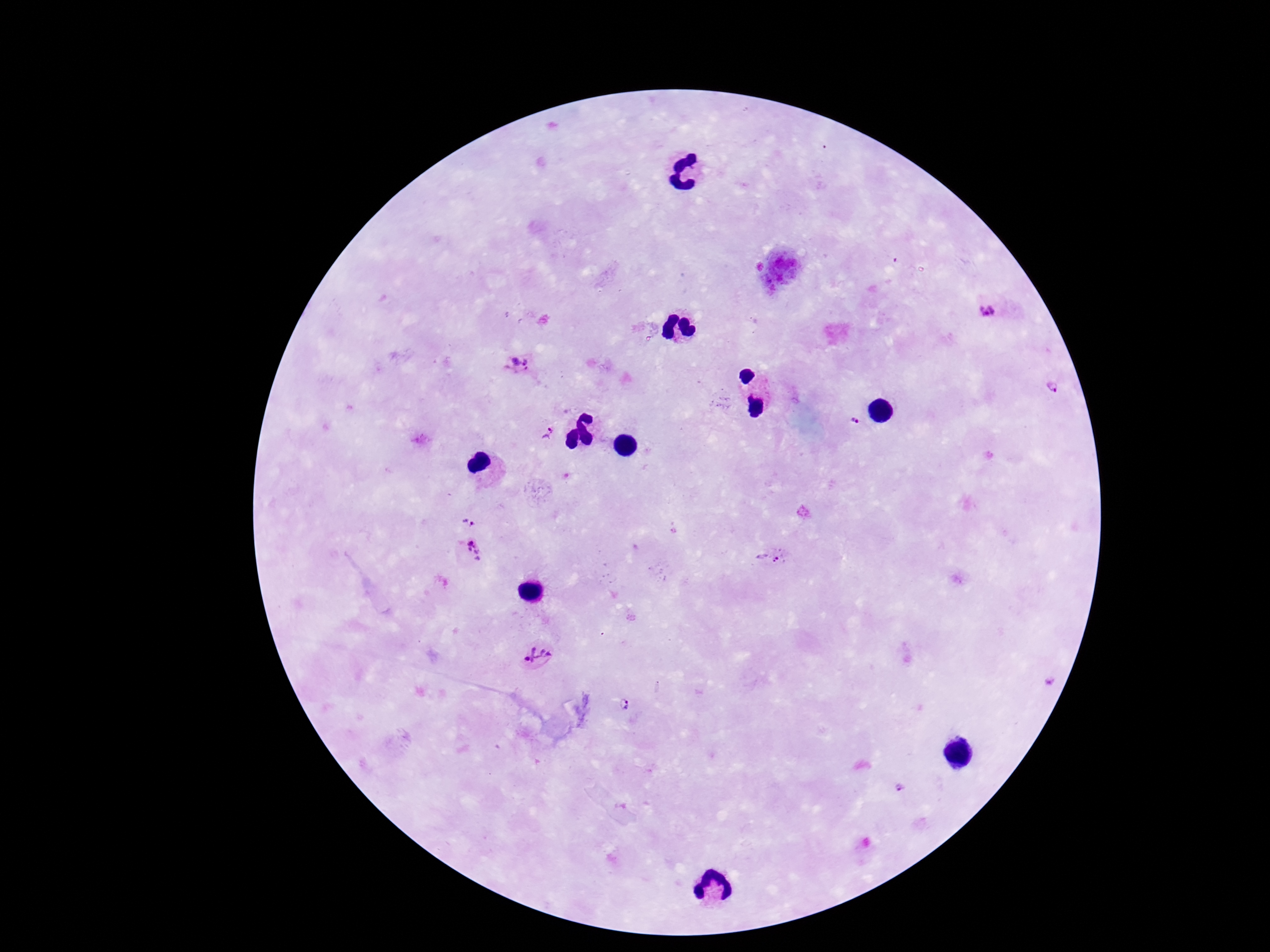
Approximate object centers, in pixels from the top-left corner.
Summary:
  - Plasmodium parasite locations: (x=988, y=312), (x=520, y=364), (x=1053, y=384), (x=855, y=422), (x=549, y=433), (x=471, y=520), (x=471, y=551), (x=770, y=557), (x=536, y=654), (x=1051, y=682), (x=627, y=705), (x=902, y=788)
  - Magnification: 100x
  - Preparation: thick blood smear
  - Capture: smartphone camera through the microscope eyepiece
  - Stain: Giemsa
  - Field of view: one from this slide
  - Image size: 1270×952 pixels
  - Patient malaria status: positive